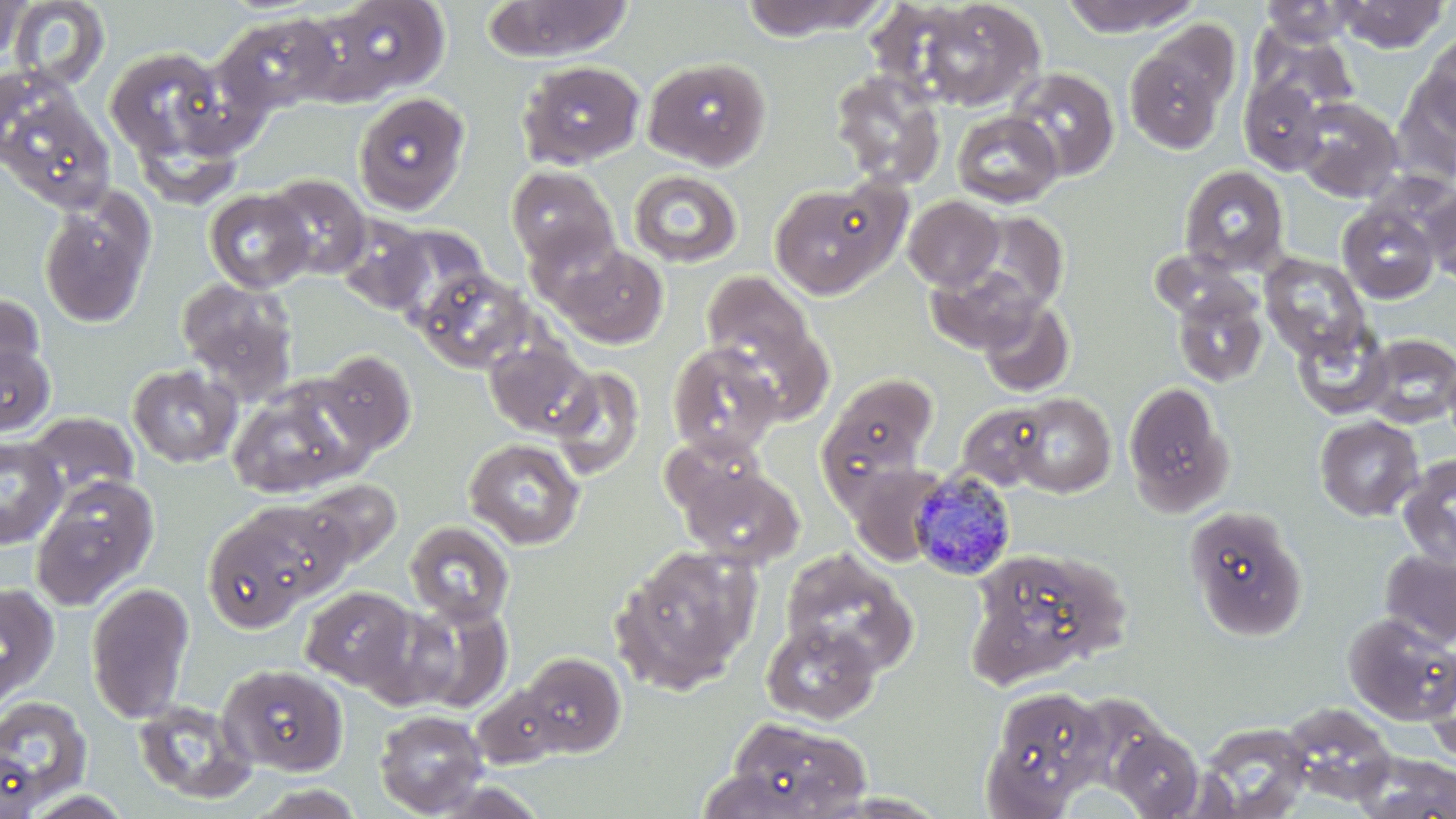
plasmodium_malariae_infected_red_blood_cell_locations: 'approximate bounding boxes as (x1,y1)-(x2,y2) corner pairs in pixels: (909,471)-(1019,582)'
slide_level_diagnosis: Plasmodium malariae
image_size: 1456×819 pixels
field_of_view: one of a larger specimen
uninfected_red_blood_cell_locations: 'approximate bounding boxes as (x1,y1)-(x2,y2) corner pairs in pixels: (0,0)-(29,67), (5,0)-(111,92), (314,0)-(451,101), (738,0)-(888,40), (907,0)-(1046,111), (1059,0)-(1205,36), (1335,0)-(1450,52), (483,1)-(633,62), (1259,1)-(1358,47), (212,12)-(344,117), (1249,29)-(1358,118), (1124,31)-(1234,153), (1418,31)-(1455,141), (103,45)-(244,174), (643,56)-(771,170), (517,60)-(645,169), (1006,67)-(1120,181), (828,70)-(946,189), (1393,70)-(1456,186), (0,72)-(116,214), (1239,77)-(1329,175), (353,92)-(470,214), (1294,97)-(1403,202), (952,111)-(1063,207), (505,165)-(620,271), (1179,165)-(1290,275), (628,170)-(742,268), (261,174)-(372,280), (769,180)-(902,299), (1420,185)-(1456,289), (38,188)-(157,329), (203,188)-(316,292), (903,196)-(1004,291), (1337,203)-(1440,304), (964,211)-(1069,315), (334,216)-(433,314), (551,244)-(669,348), (1259,252)-(1371,361), (926,262)-(1041,354), (417,268)-(536,374), (702,269)-(817,381), (175,276)-(299,399), (1170,285)-(1268,388), (0,291)-(47,399), (977,297)-(1076,397), (1292,323)-(1393,420), (1358,333)-(1456,427), (484,339)-(597,438), (0,340)-(55,438), (666,341)-(783,460), (1441,349)-(1456,457), (317,350)-(416,456), (127,363)-(242,468), (547,364)-(646,481), (826,372)-(937,475), (226,379)-(368,498), (1122,381)-(1235,517), (1010,393)-(1116,497), (956,403)-(1054,491), (25,412)-(139,505), (1315,415)-(1423,521), (660,432)-(771,523), (0,435)-(65,548), (463,438)-(585,549), (1397,453)-(1456,571), (678,464)-(803,568), (30,475)-(159,611), (299,479)-(401,567), (236,499)-(356,603), (1184,505)-(1307,641), (200,512)-(319,633), (405,521)-(514,625), (611,544)-(762,694), (966,546)-(1129,684), (779,548)-(918,677), (1379,549)-(1456,649), (0,582)-(60,708), (86,582)-(195,723), (300,586)-(417,689), (398,599)-(513,711), (1343,613)-(1456,724), (762,622)-(880,724), (517,652)-(626,756), (1422,653)-(1456,766), (218,663)-(349,776), (471,683)-(568,767), (983,686)-(1111,813), (0,695)-(93,814), (131,699)-(258,805), (374,709)-(489,816), (722,716)-(871,818), (1195,722)-(1313,818), (1108,726)-(1206,817), (0,750)-(42,819), (1352,753)-(1456,818), (418,779)-(549,818), (244,784)-(368,819), (16,789)-(138,819)'
preparation: thin blood film
modality: light microscopy
stain: May-Grünwald-Giemsa
magnification: 1000x